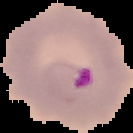
{
  "image_type": "segmented cell region with the area outside set to black",
  "malaria_status": "parasitized",
  "preparation": "thin blood film",
  "image_size": "133×133 pixels"
}